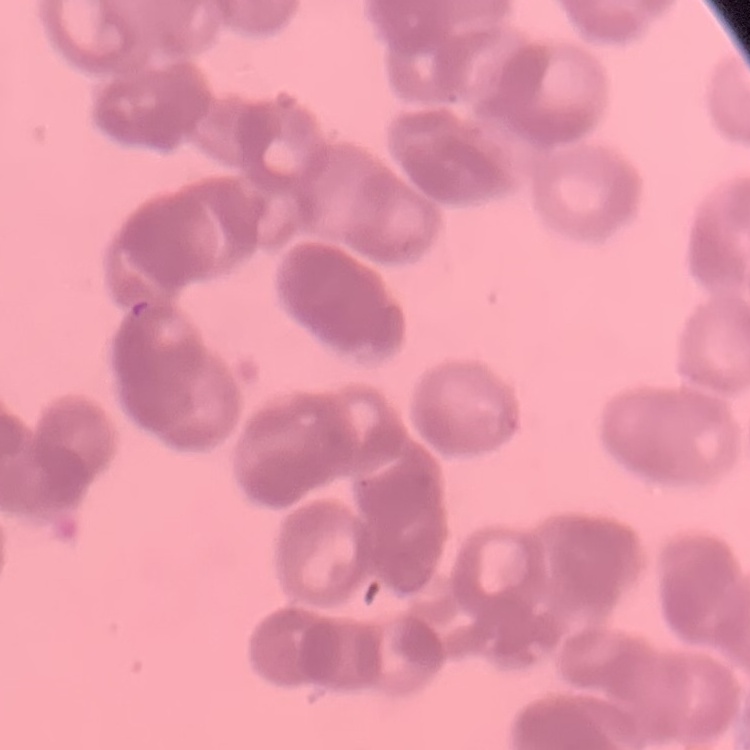

The erythrocytes exhibit rouleaux formation. Field's or Giemsa stain. One tile cut from a larger photomicrograph. Thin peripheral smear.